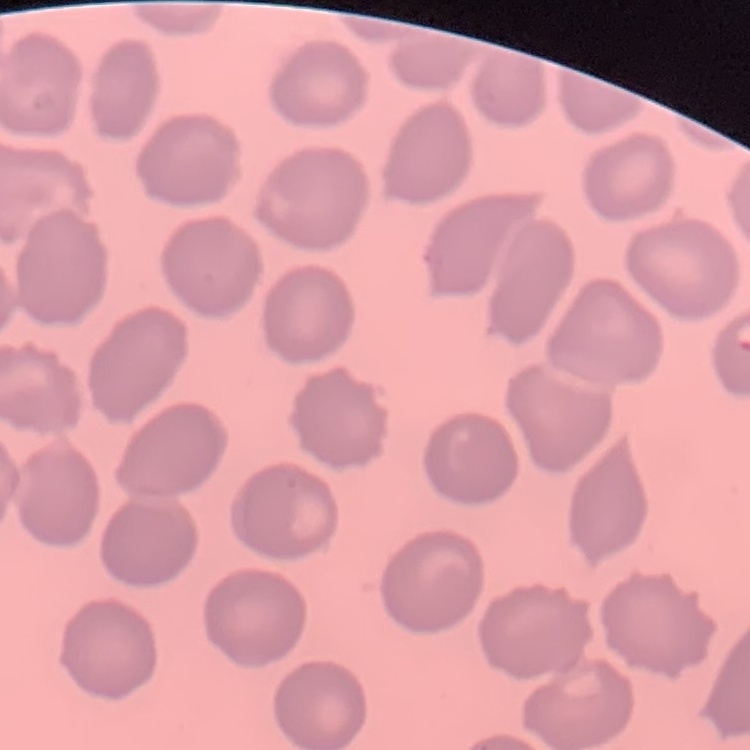

Summary:
  - Erythrocyte morphology: no rouleaux formation
  - Stain: Field's or Giemsa
  - Preparation: thin peripheral smear
  - Image type: square crop of a larger photomicrograph